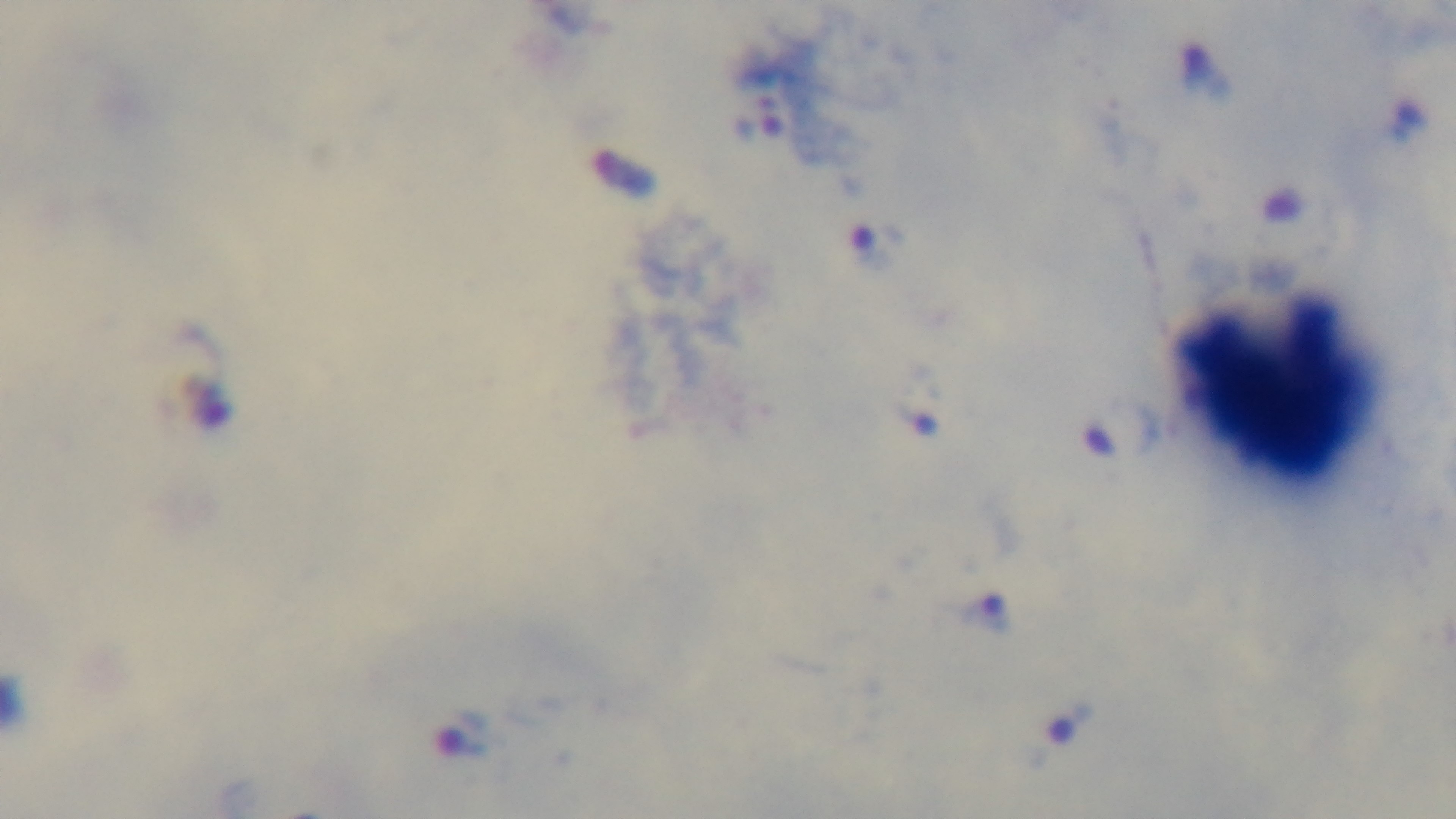 Malaria status: positive. Single field of view. Photomicrograph. Mounted 4K digital camera. Preparation: thick smear. Oil-immersion objective, 100x. Giemsa stain.